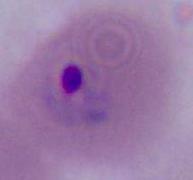

modality: micrograph
identification: Plasmodium
magnification: 400x or 1000x